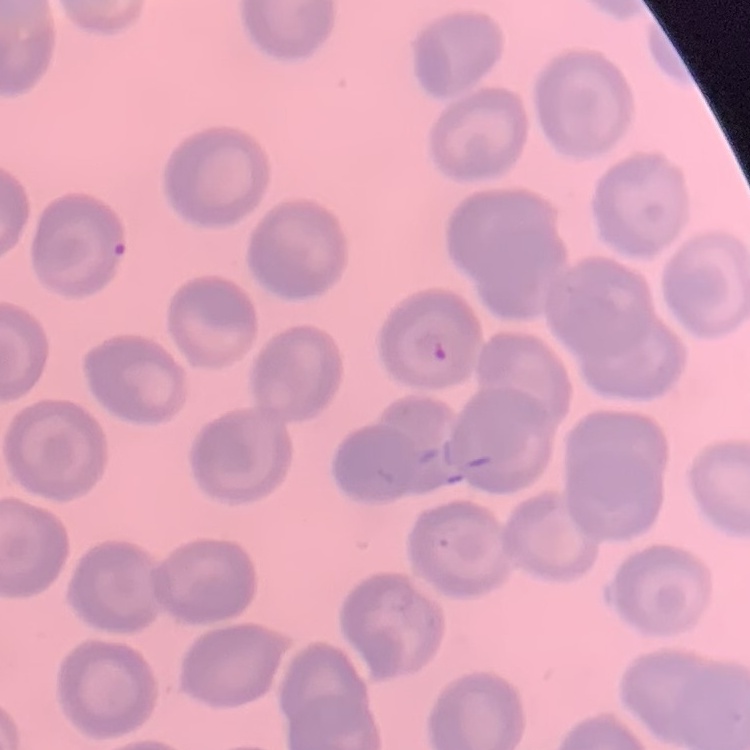

red blood cell morphology = no rouleaux formation
stain = Field's or Giemsa
image type = square crop of a larger photomicrograph
preparation = thin blood smear